Comment on the morphology of the erythrocytes.
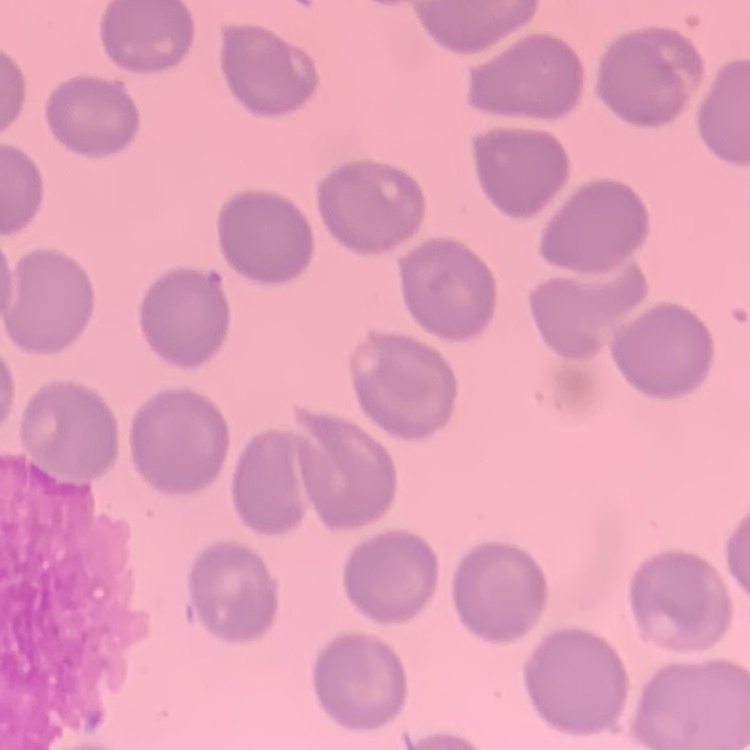

They show no rouleaux formation.

stain: Field's or Giemsa
image_type: one tile cut from a larger photomicrograph
preparation: thin peripheral smear